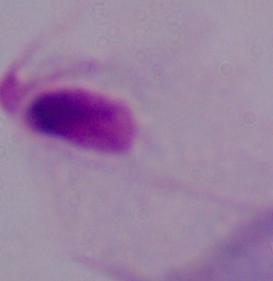
Photomicrograph. A trichomonad is shown. Captured at 1000x magnification.